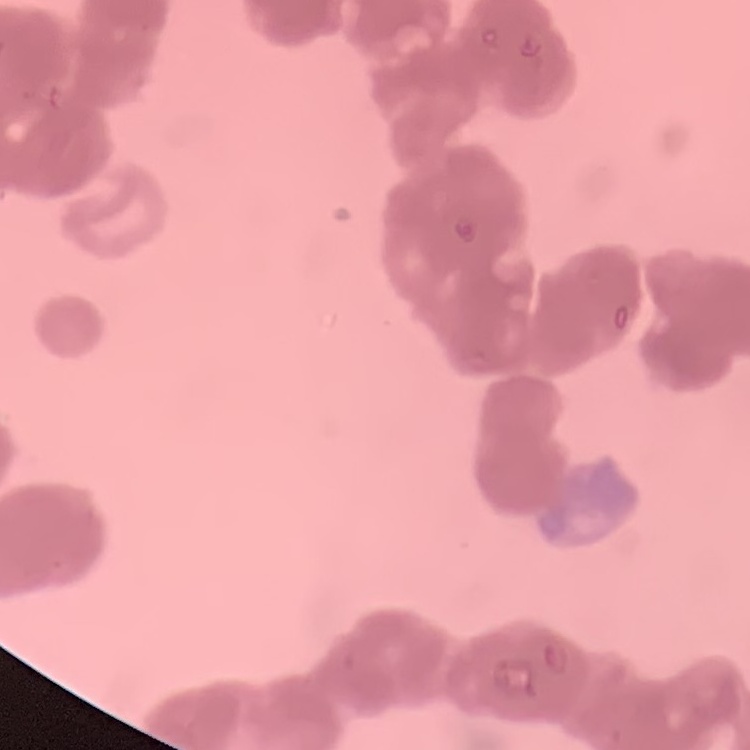 The erythrocytes exhibit rouleaux formation. One tile cut from a larger photomicrograph. Field's or Giemsa stain. Thin blood film.